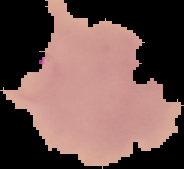
Summary:
  - Preparation: thin blood smear
  - Image type: cell region segmented out of the field of view; surrounding area masked to black
  - Image size: 184×169 pixels
  - Malaria status: parasitized